Assess this cell for malaria.
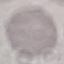
Uninfected.

Summary:
  - Capture: smartphone camera at the microscope eyepiece
  - Stain: Giemsa
  - Preparation: thin blood film
  - Image type: cell patch, automatically extracted from a larger field of view and resized to 64 × 64 pixels